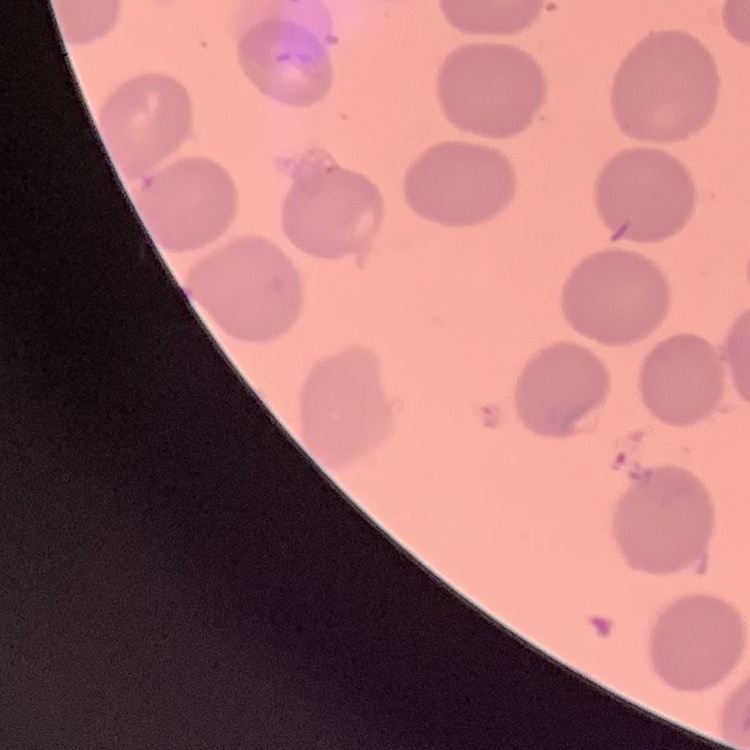
The erythrocytes show no rouleaux formation. Field's or Giemsa stain. Square crop of a larger photomicrograph. Thin blood film.